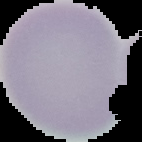

Segmented cell region on a black background. Result: no Plasmodium parasites detected. From a thin blood film. Image is 142×142 pixels.